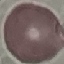

Malaria status: uninfected. Giemsa-stained preparation. Thin blood smear. Acquired by smartphone through the microscope eyepiece. Automatically extracted cell patch, resized to 64 × 64 pixels.